Identify the parasite.
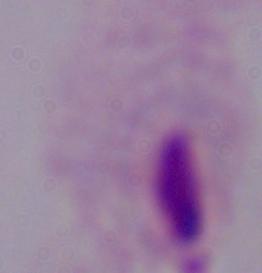

A trichomonad.

modality: micrograph
magnification: 1000x